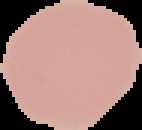

Cell region segmented out of the field of view; the surrounding area is masked to black. Image is 142×130 pixels. Result: no Plasmodium parasites seen. From a thin blood film.